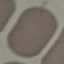
Summary:
  - Result: no malaria parasites detected
  - Image type: cell patch, automatically extracted from a larger field of view and resized to 64 × 64 pixels
  - Preparation: thin blood film
  - Stain: Giemsa
  - Capture: smartphone through the microscope eyepiece